State the blood parasite species.
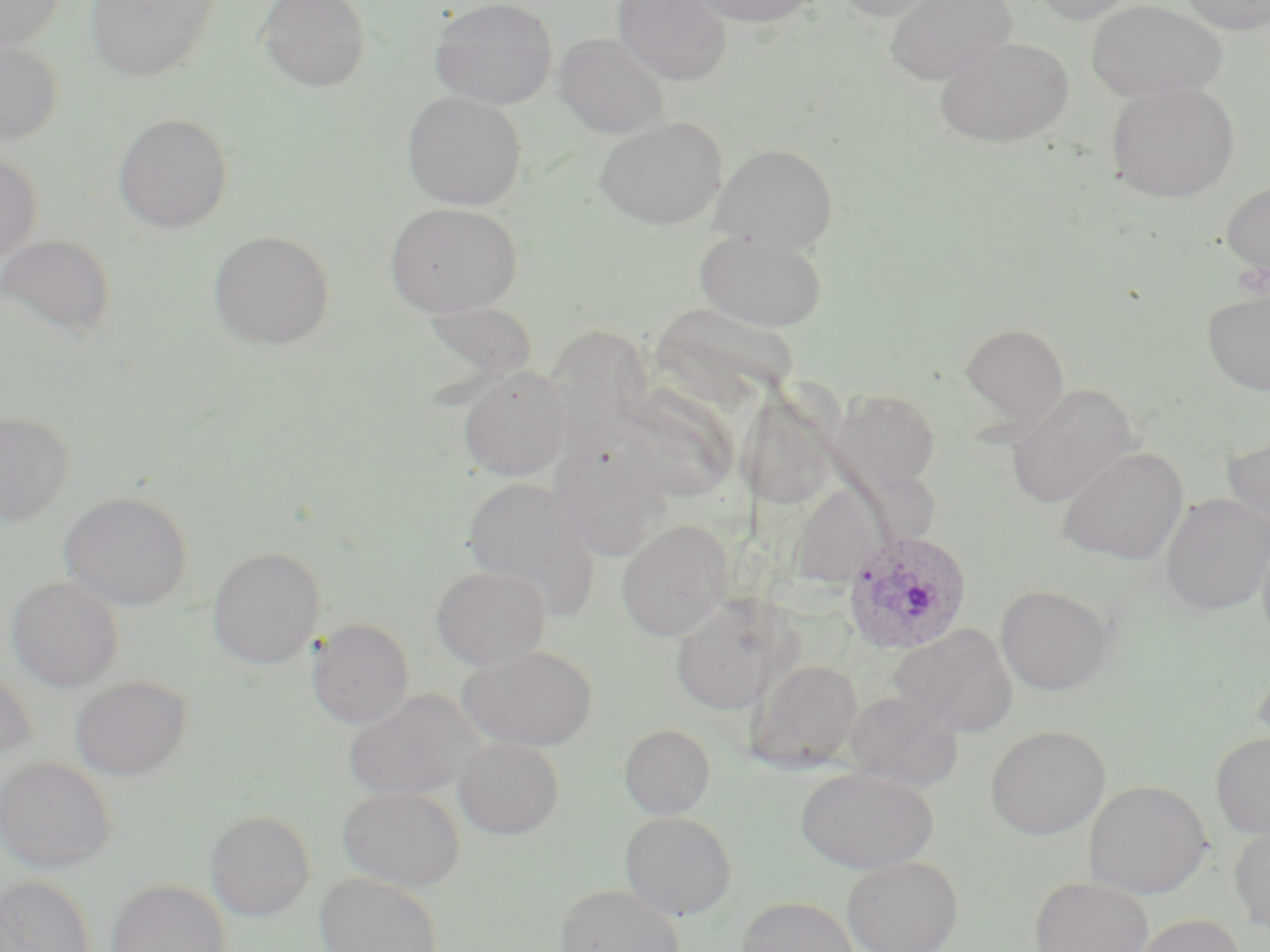

Plasmodium ovale.

uninfected red blood cell locations = approximate bounding boxes as (x1, y1, x2, y2) in pixels: (0, 0, 67, 52), (85, 0, 220, 81), (257, 0, 371, 91), (429, 0, 558, 109), (612, 0, 733, 85), (689, 0, 821, 27), (833, 0, 945, 20), (884, 0, 1017, 84), (1032, 0, 1139, 25), (1086, 0, 1227, 103), (1179, 0, 1270, 34), (555, 33, 670, 138), (0, 36, 62, 144), (934, 36, 1075, 146), (1105, 82, 1240, 202), (401, 90, 527, 210), (113, 113, 234, 233), (594, 117, 727, 228), (709, 143, 838, 253), (0, 152, 41, 264), (1221, 179, 1270, 280), (384, 201, 523, 317), (693, 228, 829, 331), (207, 230, 335, 349), (0, 233, 117, 341), (1201, 288, 1270, 397), (650, 302, 801, 405), (959, 322, 1069, 427), (550, 324, 658, 450), (458, 366, 572, 481), (1004, 383, 1140, 509), (832, 387, 942, 497), (626, 390, 738, 507), (738, 392, 839, 511), (1, 412, 74, 526), (1221, 432, 1270, 531), (549, 442, 671, 562), (1056, 446, 1189, 565), (462, 477, 601, 618), (789, 482, 884, 589), (58, 491, 192, 611), (1161, 493, 1270, 615), (616, 519, 734, 641), (1257, 528, 1270, 654), (207, 547, 325, 669), (431, 566, 551, 671), (7, 575, 124, 692), (996, 584, 1115, 695), (670, 598, 786, 716), (307, 617, 414, 729), (890, 623, 1018, 737), (458, 645, 598, 751), (747, 657, 864, 772), (1251, 658, 1270, 756), (0, 662, 36, 764), (71, 675, 192, 779), (343, 689, 487, 801), (845, 691, 964, 791), (619, 723, 716, 819), (986, 724, 1110, 839), (1210, 732, 1270, 839), (454, 736, 564, 839), (0, 756, 117, 872), (796, 767, 938, 874), (1083, 779, 1212, 898), (337, 786, 466, 890), (205, 810, 315, 921), (619, 810, 737, 920), (1229, 824, 1270, 931), (842, 856, 963, 952), (315, 872, 443, 952), (0, 874, 96, 952), (1030, 876, 1154, 952), (107, 879, 230, 952), (553, 883, 687, 952), (735, 896, 861, 952), (1129, 913, 1246, 952)
field of view = single
Plasmodium ovale-infected red blood cell locations = approximate bounding boxes as (x1, y1, x2, y2) in pixels: (843, 530, 972, 655)
modality = optical microscopy
image size = 1270×952 pixels
magnification = 1000x
stain = May-Grünwald-Giemsa
preparation = thin blood film